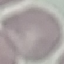

malaria_status: uninfected
capture: smartphone through the microscope eyepiece
stain: Giemsa
preparation: thin blood smear
image_type: cell patch, automatically extracted from a larger field of view and resized to 64 × 64 pixels